State which cell type is depicted.
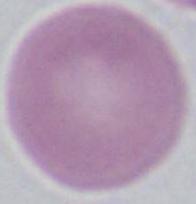

This is an erythrocyte.

Photomicrograph. Captured at 1000x magnification.